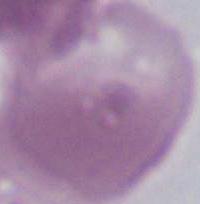

An erythrocyte is seen. Captured at 1000x magnification. Photomicrograph.